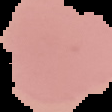
{
  "preparation": "thin blood smear",
  "image_size": "112×112 pixels",
  "image_type": "segmented cell region on a black background",
  "malaria_status": "uninfected"
}